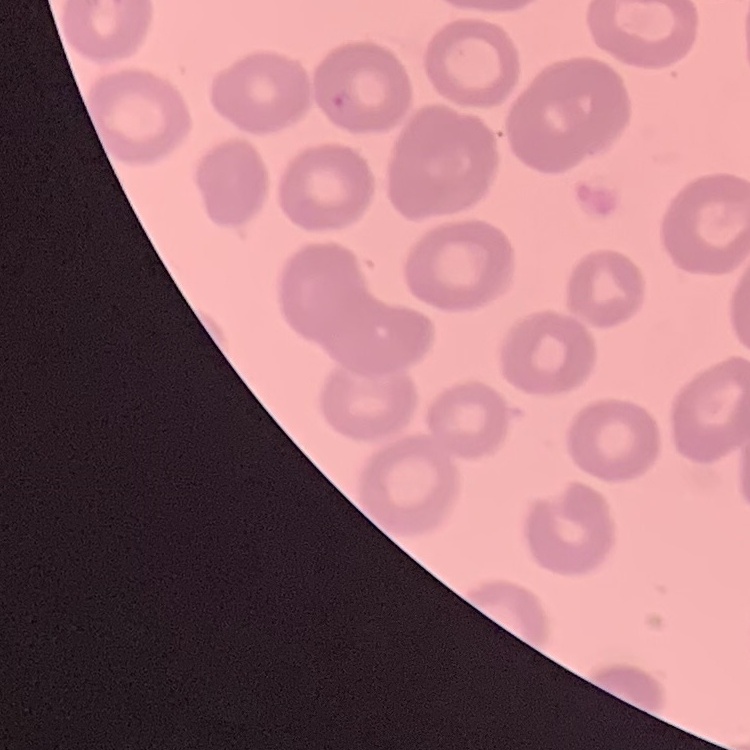

red blood cell morphology = no rouleaux formation
stain = Field's or Giemsa
image type = square crop of a larger photomicrograph
preparation = thin peripheral smear